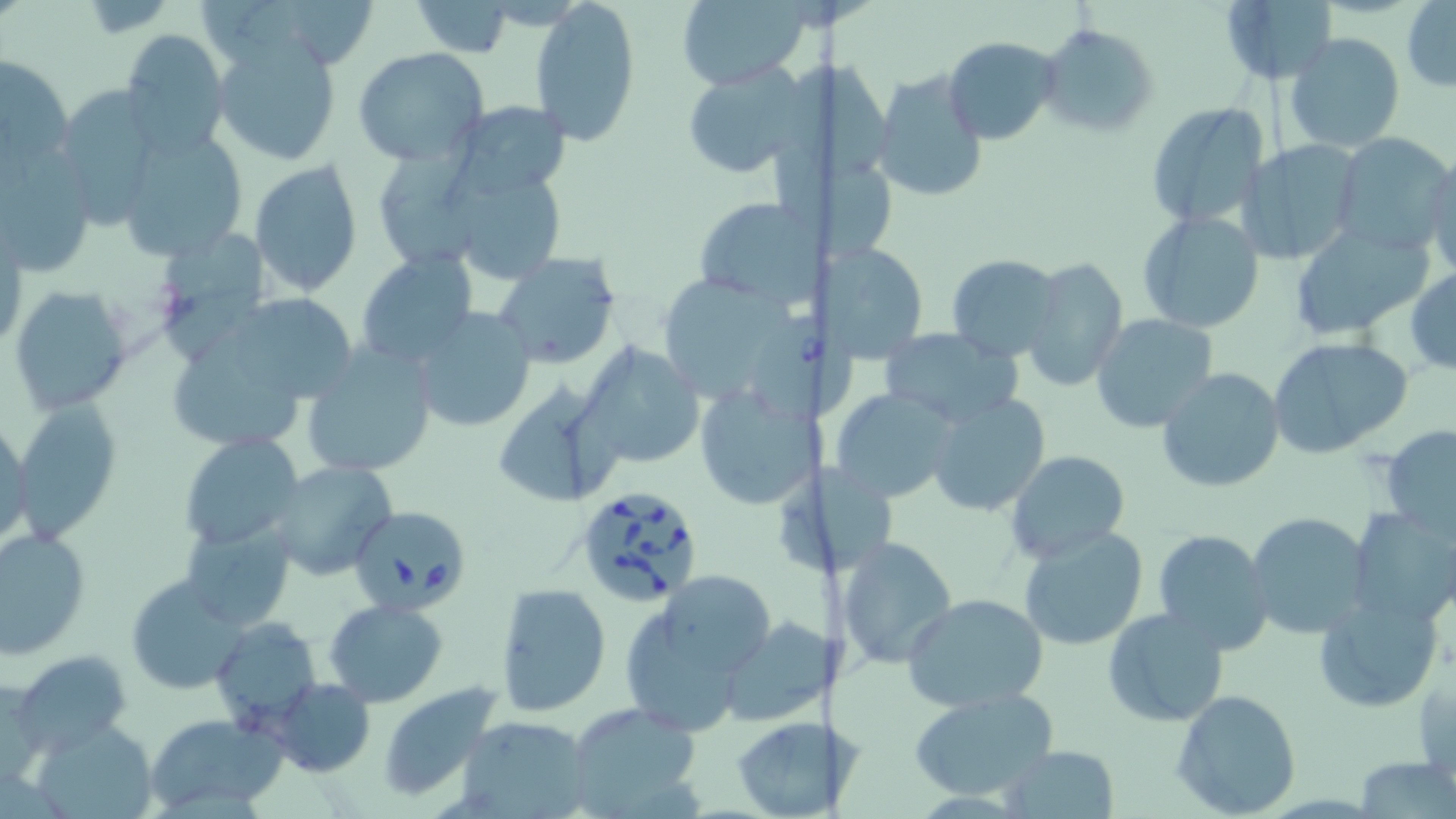
slide_level_diagnosis: Babesia divergens
stain: May-Grünwald-Giemsa
babesia_divergens_infected_red_blood_cell_locations: 'approximate bounding boxes as (x1, y1, x2, y2) in pixels: (752, 317, 854, 415), (574, 484, 706, 607), (355, 509, 470, 617)'
uninfected_red_blood_cell_locations: 'approximate bounding boxes as (x1, y1, x2, y2) in pixels: (531, 0, 642, 146), (675, 0, 808, 89), (1218, 0, 1337, 86), (409, 1, 517, 56), (1402, 1, 1455, 92), (1039, 23, 1159, 140), (118, 29, 230, 157), (1284, 33, 1405, 154), (211, 34, 344, 167), (945, 35, 1062, 144), (353, 48, 491, 164), (1, 54, 74, 174), (785, 56, 901, 183), (688, 62, 815, 174), (871, 68, 988, 202), (53, 85, 165, 227), (449, 100, 572, 200), (1146, 100, 1270, 233), (120, 129, 250, 263), (1331, 131, 1453, 255), (1240, 141, 1362, 265), (778, 145, 903, 267), (381, 146, 478, 270), (1423, 155, 1456, 278), (249, 160, 363, 296), (443, 165, 570, 286), (692, 196, 819, 310), (1137, 211, 1264, 334), (1287, 221, 1432, 338), (160, 231, 267, 366), (828, 242, 928, 363), (355, 251, 478, 368), (491, 251, 622, 369), (948, 254, 1063, 362), (1021, 255, 1128, 394), (1407, 267, 1456, 376), (661, 278, 802, 403), (7, 284, 131, 415), (224, 289, 370, 401), (411, 307, 537, 433), (1089, 312, 1219, 433), (880, 327, 1024, 428), (175, 332, 301, 444), (1265, 336, 1413, 458), (579, 339, 704, 469), (300, 344, 439, 479), (1155, 365, 1284, 493), (692, 376, 820, 513), (492, 379, 625, 508), (831, 385, 960, 504), (926, 391, 1050, 517), (12, 397, 123, 539), (1, 418, 32, 551), (1380, 427, 1456, 537), (180, 434, 304, 551), (1006, 450, 1130, 563), (267, 462, 398, 581), (778, 466, 895, 571), (1348, 508, 1456, 628), (1244, 511, 1372, 639), (180, 520, 296, 631), (1, 526, 91, 658), (1018, 526, 1148, 651), (1153, 528, 1274, 654), (838, 535, 956, 669), (123, 574, 250, 694), (663, 579, 771, 671), (496, 582, 612, 716), (903, 593, 1048, 711), (1313, 593, 1441, 712), (324, 598, 448, 705), (626, 605, 735, 735), (1102, 606, 1229, 729), (212, 617, 320, 732), (719, 617, 827, 729), (14, 651, 132, 752), (268, 677, 375, 777), (377, 682, 504, 804), (1169, 688, 1303, 818), (906, 689, 1062, 803), (568, 702, 702, 816), (140, 713, 279, 814), (455, 715, 594, 819), (34, 717, 157, 818), (732, 717, 832, 819), (1002, 744, 1120, 816), (1354, 755, 1455, 818)'
field_of_view: single
image_size: 1456×819 pixels
modality: light microscopy
magnification: 1000x
preparation: thin blood smear